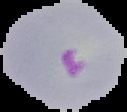
Summary:
  - Image type: segmented cell region with the area outside set to black
  - Result: malaria parasites detected
  - Preparation: thin blood film
  - Image size: 127×112 pixels